Locate every uninfected red blood cell.
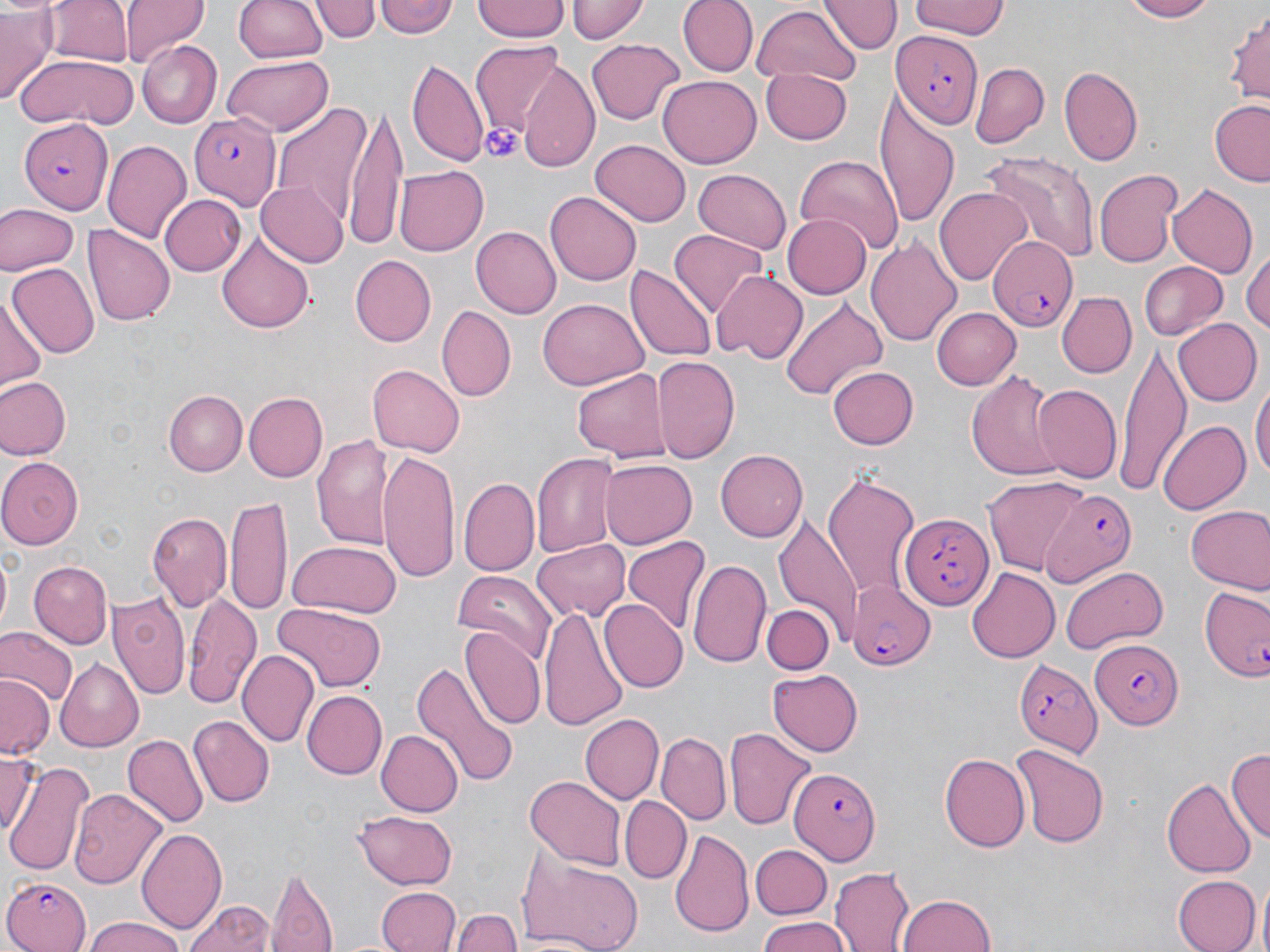
Approximate bounding boxes as (x1, y1, x2, y2) in pixels.
Uninfected red blood cells: (121, 0, 210, 70), (230, 0, 329, 62), (316, 0, 380, 43), (374, 0, 457, 39), (472, 0, 571, 43), (566, 0, 647, 43), (679, 0, 755, 77), (823, 0, 896, 54), (910, 0, 1012, 40), (1115, 0, 1222, 22), (46, 1, 131, 67), (0, 5, 57, 102), (752, 5, 857, 87), (1226, 8, 1270, 107), (584, 39, 685, 125), (136, 40, 222, 130), (470, 42, 567, 135), (18, 53, 137, 130), (223, 54, 335, 134), (408, 56, 487, 165), (970, 61, 1051, 148), (520, 64, 602, 174), (1059, 66, 1145, 167), (761, 68, 853, 144), (658, 74, 760, 168), (268, 96, 374, 229), (874, 100, 960, 230), (1208, 100, 1270, 184), (344, 107, 410, 252), (104, 140, 193, 242), (591, 140, 690, 227), (979, 152, 1100, 264), (793, 154, 905, 253), (394, 166, 487, 256), (693, 167, 791, 254), (1094, 167, 1184, 268), (256, 180, 349, 268), (1167, 182, 1259, 280), (934, 187, 1031, 284), (547, 189, 640, 283), (158, 195, 245, 277), (0, 204, 77, 276), (784, 215, 869, 298), (83, 226, 175, 327), (470, 226, 560, 318), (215, 227, 314, 336), (669, 229, 768, 317), (866, 233, 963, 347), (1243, 252, 1270, 338), (348, 256, 434, 346), (1138, 260, 1228, 341), (7, 265, 98, 359), (627, 265, 717, 365), (710, 268, 808, 361), (1058, 292, 1136, 377), (0, 294, 47, 390), (777, 296, 888, 401), (538, 298, 646, 391), (437, 306, 516, 404), (932, 306, 1021, 390), (1170, 318, 1261, 407), (1119, 343, 1192, 496), (651, 356, 739, 466), (827, 365, 918, 450), (368, 366, 462, 456), (572, 367, 671, 463), (966, 369, 1068, 479), (986, 370, 1107, 529), (0, 378, 70, 460), (1033, 383, 1122, 484), (1252, 383, 1269, 484), (165, 390, 246, 476), (243, 391, 326, 483), (1157, 420, 1249, 515), (311, 431, 393, 548), (378, 447, 462, 587), (715, 449, 807, 543), (532, 453, 618, 557), (0, 455, 82, 548), (601, 460, 697, 548), (822, 472, 920, 603), (459, 476, 540, 578), (983, 477, 1087, 576), (225, 495, 292, 615), (1186, 506, 1270, 594), (147, 510, 231, 615), (774, 510, 863, 642), (623, 537, 709, 635), (532, 540, 629, 623), (287, 542, 399, 618), (688, 556, 773, 669), (27, 560, 113, 647), (1059, 564, 1170, 654), (454, 569, 556, 662), (965, 569, 1061, 663), (109, 590, 190, 702), (183, 591, 260, 706), (599, 599, 688, 692), (272, 603, 386, 690), (762, 605, 835, 674), (541, 606, 627, 733), (0, 626, 77, 707), (459, 627, 545, 732), (237, 649, 319, 746), (405, 655, 521, 791), (55, 660, 146, 751), (769, 667, 863, 755), (0, 676, 55, 761), (303, 690, 386, 778), (581, 714, 664, 804), (189, 716, 273, 807), (723, 727, 817, 833), (375, 729, 462, 817), (657, 733, 730, 823), (122, 734, 207, 827), (1009, 742, 1109, 846), (1227, 747, 1270, 846), (941, 751, 1031, 851), (0, 753, 38, 843), (4, 757, 90, 876), (526, 775, 625, 870), (1162, 781, 1255, 876), (69, 787, 167, 891), (620, 795, 692, 881), (352, 809, 457, 888), (137, 828, 227, 937), (670, 828, 754, 939), (750, 844, 829, 917), (520, 851, 645, 952), (834, 867, 916, 952), (267, 868, 340, 952), (1171, 875, 1259, 952), (375, 887, 460, 952), (897, 893, 997, 952), (185, 898, 276, 952), (451, 908, 523, 952), (754, 918, 853, 952), (81, 919, 191, 952).

Platelet locations: (479, 122, 524, 163). Plasmodium falciparum-infected red blood cell locations: (896, 30, 984, 126), (190, 112, 281, 207), (20, 116, 114, 211), (988, 233, 1083, 334), (1039, 488, 1135, 588), (900, 511, 991, 612), (848, 582, 934, 671), (1202, 587, 1270, 681), (1090, 636, 1182, 726), (1011, 655, 1101, 756), (788, 766, 879, 867), (2, 874, 93, 952). Slide-level diagnosis: Plasmodium falciparum. May-Grünwald-Giemsa stain. Image is 1270×952 pixels. Single field of view. Captured at 1000x magnification. Thin blood film. Optical microscopy.